Describe the morphology of the red blood cells.
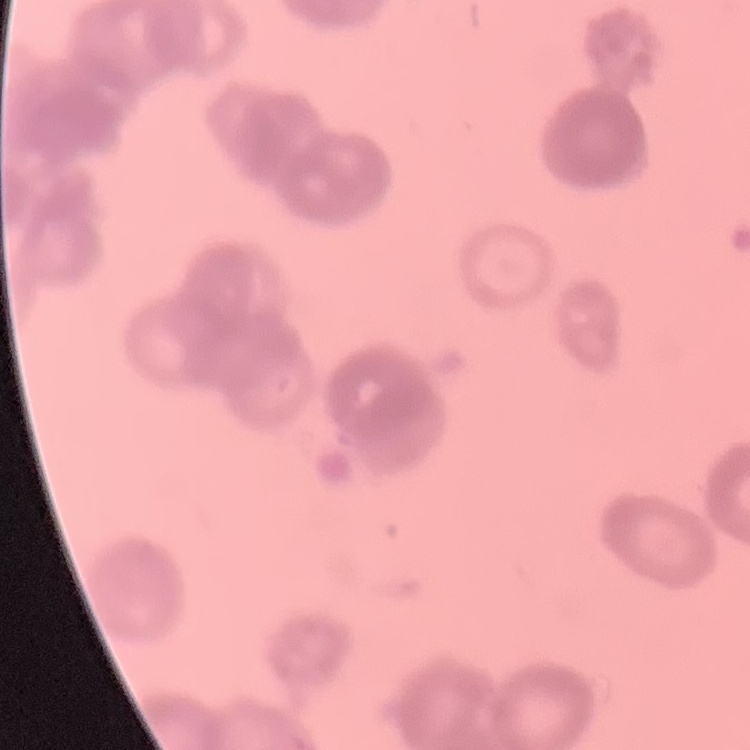

Rouleaux formation.

One tile cut from a larger photomicrograph. Thin blood film. Field's or Giemsa stain.